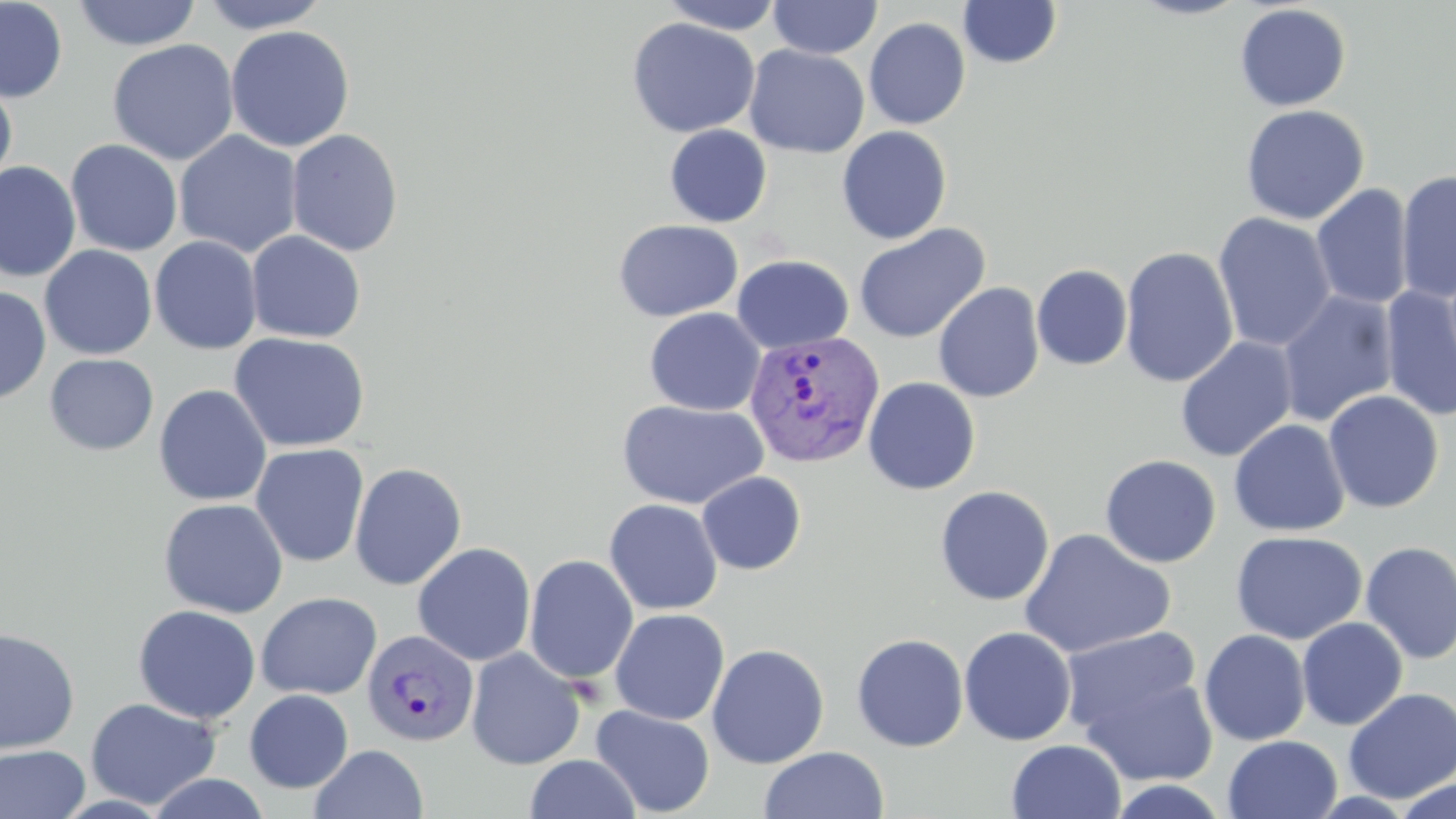
slide-level diagnosis = Plasmodium vivax
field of view = one of a larger specimen
stain = May-Grünwald-Giemsa
magnification = 1000x
image size = 1456×819 pixels
uninfected red blood cell locations = approximate bounding boxes as (x1,y1)-(x2,y2) corner pairs in pixels: (0,0)-(68,104), (198,0)-(332,34), (657,0)-(786,35), (767,0)-(882,59), (1126,0)-(1253,21), (71,1)-(202,51), (957,1)-(1063,69), (1234,4)-(1352,112), (626,17)-(760,138), (863,17)-(970,129), (225,25)-(355,152), (107,38)-(239,165), (744,45)-(870,158), (0,74)-(17,191), (1240,104)-(1370,225), (664,125)-(772,228), (836,125)-(952,244), (286,128)-(404,257), (174,130)-(302,258), (65,139)-(183,256), (0,162)-(81,282), (1395,169)-(1456,305), (1311,184)-(1413,310), (1213,212)-(1337,353), (613,219)-(743,322), (853,224)-(991,343), (246,230)-(366,343), (149,235)-(262,355), (40,245)-(157,360), (1119,246)-(1238,387), (732,254)-(855,354), (1032,264)-(1133,371), (933,282)-(1045,403), (0,285)-(51,404), (1379,285)-(1456,421), (1277,290)-(1399,427), (644,307)-(766,416), (228,332)-(371,453), (1175,336)-(1297,462), (45,353)-(159,455), (862,377)-(981,495), (153,384)-(272,507), (1322,389)-(1444,513), (617,399)-(769,511), (1228,419)-(1350,537), (250,443)-(369,568), (1099,455)-(1222,568), (349,462)-(467,590), (697,471)-(807,575), (934,485)-(1055,606), (158,498)-(289,618), (604,498)-(723,615), (1018,528)-(1176,660), (1230,531)-(1366,645), (1359,540)-(1456,664), (412,542)-(536,666), (523,555)-(639,685), (256,591)-(382,699), (133,604)-(261,724), (609,608)-(730,725), (1297,617)-(1408,731), (959,626)-(1077,745), (0,627)-(80,754), (1059,627)-(1204,739), (1199,630)-(1310,746), (851,633)-(969,752), (706,643)-(830,769), (466,647)-(586,770), (1079,670)-(1220,788), (1342,688)-(1456,803), (244,689)-(353,793), (85,697)-(221,810), (591,705)-(715,817), (1222,735)-(1342,819), (1007,740)-(1126,819), (0,744)-(90,819), (310,744)-(428,819), (759,746)-(889,819), (524,753)-(640,819), (145,772)-(271,818), (1393,778)-(1456,818), (1105,779)-(1231,818)
preparation = thin blood smear
Plasmodium vivax-infected red blood cell locations = approximate bounding boxes as (x1,y1)-(x2,y2) corner pairs in pixels: (743,329)-(885,469), (361,629)-(479,747)
modality = optical microscopy